Identify the parasite.
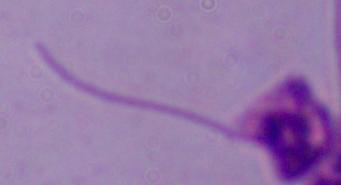
Leishmania.

magnification: 1000x
modality: photomicrograph